Name the cell type shown.
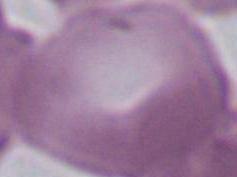
An erythrocyte.

modality = photomicrograph
magnification = 1000x